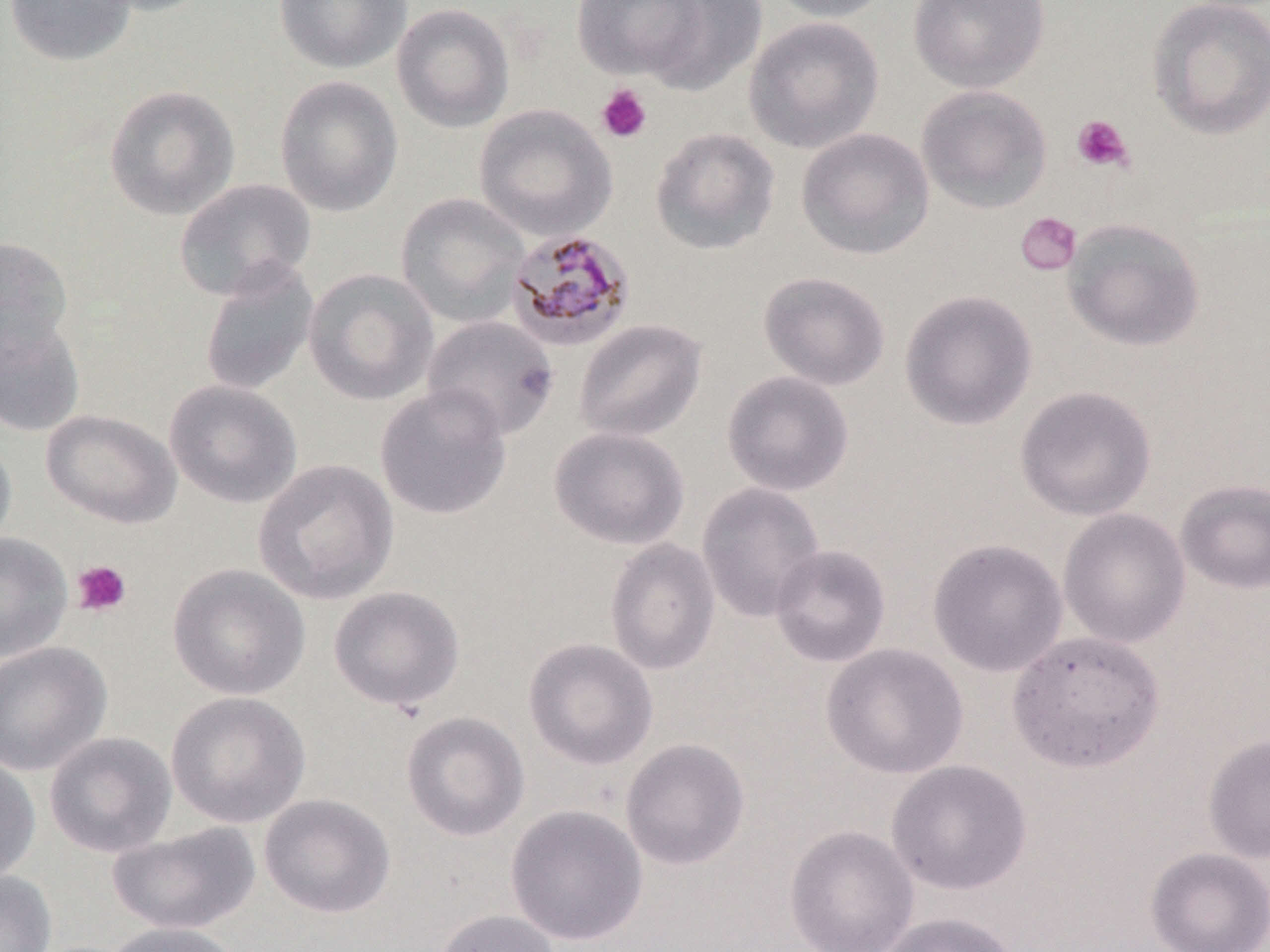

Approximate bounding boxes as (x1, y1, x2, y2) in pixels. Plasmodium malariae-infected red blood cell locations: (505, 228, 637, 352). Platelet locations: (596, 83, 653, 143), (1071, 114, 1134, 173), (1015, 211, 1082, 276), (71, 559, 132, 617). Uninfected red blood cell locations: (3, 0, 138, 67), (84, 0, 214, 17), (273, 0, 412, 74), (573, 0, 704, 81), (765, 0, 895, 23), (908, 0, 1050, 92), (1147, 0, 1270, 140), (640, 1, 766, 95), (391, 3, 515, 133), (744, 16, 884, 153), (275, 75, 403, 217), (104, 84, 240, 221), (916, 84, 1053, 214), (473, 104, 617, 241), (650, 126, 781, 255), (796, 127, 935, 260), (174, 179, 317, 300), (396, 192, 531, 328), (1063, 217, 1205, 352), (0, 237, 73, 356), (198, 260, 319, 397), (303, 268, 439, 406), (758, 271, 890, 391), (899, 289, 1038, 431), (0, 309, 85, 438), (421, 315, 560, 441), (574, 318, 707, 443), (722, 370, 854, 497), (164, 379, 302, 508), (375, 383, 512, 520), (1014, 385, 1156, 521), (41, 409, 182, 529), (548, 426, 690, 550), (0, 435, 17, 553), (253, 458, 399, 605), (1175, 479, 1270, 595), (696, 482, 825, 623), (1057, 508, 1190, 648), (0, 532, 73, 662), (604, 538, 721, 676), (927, 538, 1068, 677), (769, 544, 892, 668), (167, 562, 310, 700), (328, 585, 465, 712), (1007, 629, 1165, 772), (523, 637, 659, 770), (0, 641, 112, 777), (821, 643, 968, 779), (166, 691, 311, 828), (401, 711, 530, 842), (44, 732, 177, 858), (1203, 732, 1270, 863), (620, 738, 750, 870), (0, 754, 41, 883), (886, 759, 1033, 895), (258, 793, 396, 919), (505, 805, 648, 946), (107, 822, 261, 935), (784, 824, 919, 952), (1145, 847, 1270, 952), (0, 869, 58, 952), (432, 909, 562, 952), (876, 911, 1022, 952), (102, 921, 242, 952). Slide-level diagnosis: Plasmodium malariae. May-Grünwald-Giemsa-stained preparation. Thin blood film. One field of a larger specimen. Optical microscopy. 1000x magnification. Image is 1270×952 pixels.